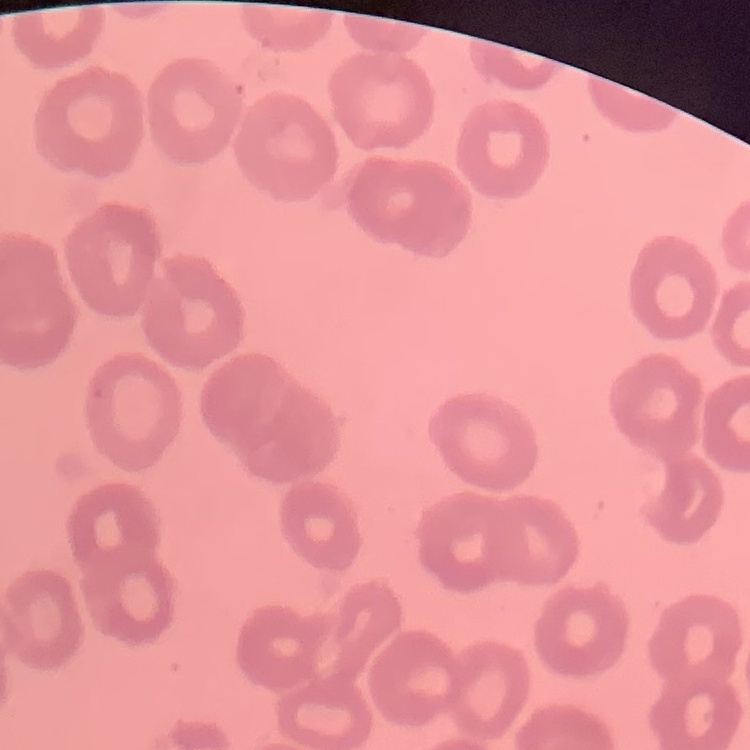

The erythrocytes show no rouleaux formation. Square crop of a larger photomicrograph. Field's or Giemsa stain. Thin blood smear.